Assess this cell for malaria.
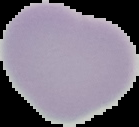
Uninfected.

Summary:
  - Image size: 139×127 pixels
  - Image type: segmented cell region on a black background
  - Preparation: thin blood smear